Describe the morphology of the red blood cells.
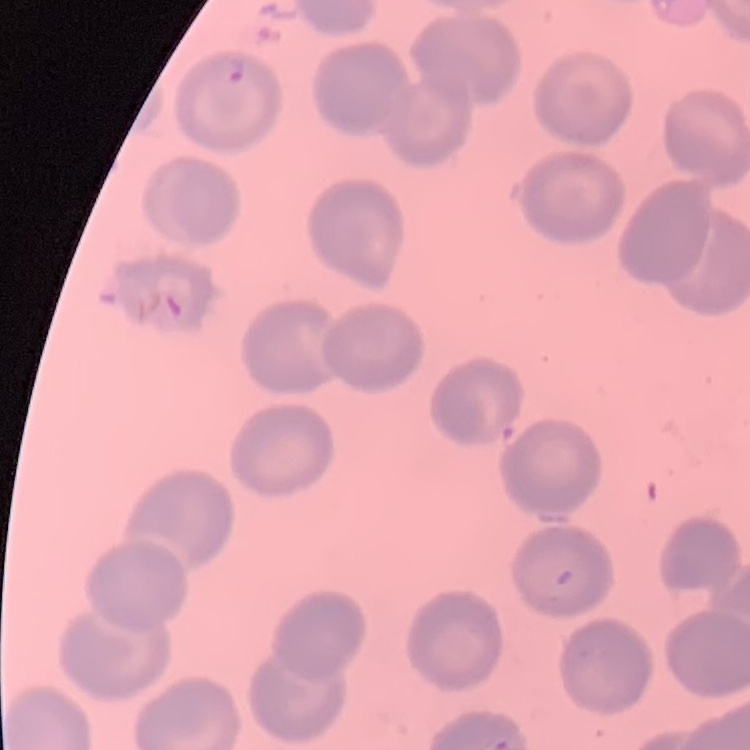

They show no rouleaux formation.

Summary:
  - Stain: Field's or Giemsa
  - Preparation: thin blood smear
  - Image type: one tile cut from a larger photomicrograph